Name the blood parasite species.
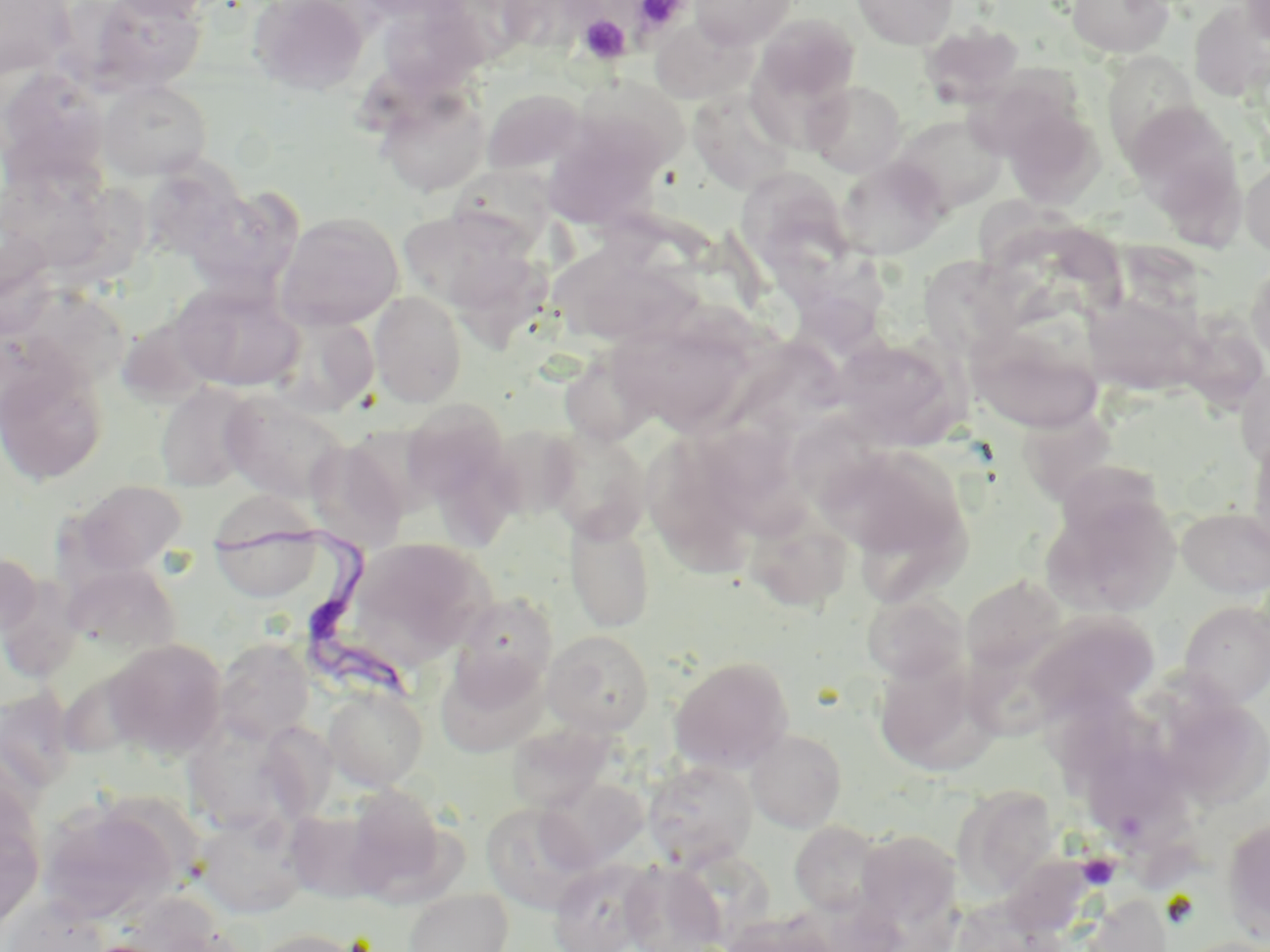

Trypanosoma brucei.

Approximate bounding boxes as named x1/y1/x2/y2 corners in pixels. Uninfected red blood cell locations: (x1=83, y1=0, x2=207, y2=92), (x1=103, y1=0, x2=221, y2=20), (x1=248, y1=0, x2=371, y2=96), (x1=689, y1=0, x2=798, y2=49), (x1=852, y1=0, x2=957, y2=50), (x1=1066, y1=0, x2=1174, y2=58), (x1=1238, y1=0, x2=1270, y2=50), (x1=0, y1=1, x2=75, y2=80), (x1=1189, y1=1, x2=1270, y2=101), (x1=375, y1=3, x2=488, y2=96), (x1=753, y1=13, x2=861, y2=110), (x1=651, y1=20, x2=757, y2=106), (x1=920, y1=23, x2=1024, y2=108), (x1=1101, y1=54, x2=1202, y2=161), (x1=0, y1=67, x2=110, y2=186), (x1=570, y1=75, x2=690, y2=178), (x1=98, y1=80, x2=213, y2=181), (x1=805, y1=80, x2=907, y2=178), (x1=374, y1=85, x2=490, y2=197), (x1=482, y1=88, x2=586, y2=176), (x1=687, y1=88, x2=798, y2=195), (x1=1124, y1=102, x2=1242, y2=212), (x1=1003, y1=105, x2=1105, y2=209), (x1=891, y1=113, x2=1008, y2=215), (x1=541, y1=115, x2=669, y2=229), (x1=835, y1=157, x2=948, y2=261), (x1=1240, y1=158, x2=1270, y2=257), (x1=0, y1=160, x2=118, y2=275), (x1=141, y1=162, x2=247, y2=262), (x1=446, y1=164, x2=559, y2=255), (x1=738, y1=172, x2=856, y2=284), (x1=184, y1=187, x2=301, y2=296), (x1=275, y1=211, x2=404, y2=330), (x1=400, y1=213, x2=547, y2=307), (x1=549, y1=256, x2=699, y2=350), (x1=1246, y1=257, x2=1270, y2=367), (x1=921, y1=262, x2=1057, y2=367), (x1=0, y1=279, x2=143, y2=395), (x1=170, y1=280, x2=304, y2=393), (x1=368, y1=290, x2=468, y2=408), (x1=1085, y1=293, x2=1204, y2=396), (x1=270, y1=311, x2=380, y2=417), (x1=1174, y1=312, x2=1270, y2=412), (x1=974, y1=333, x2=1105, y2=433), (x1=603, y1=336, x2=752, y2=427), (x1=833, y1=336, x2=962, y2=448), (x1=0, y1=359, x2=108, y2=486), (x1=1235, y1=367, x2=1270, y2=472), (x1=154, y1=382, x2=259, y2=492), (x1=219, y1=391, x2=351, y2=504), (x1=399, y1=399, x2=511, y2=512), (x1=1019, y1=416, x2=1131, y2=502), (x1=484, y1=425, x2=582, y2=521), (x1=539, y1=426, x2=653, y2=541), (x1=1247, y1=430, x2=1270, y2=559), (x1=305, y1=439, x2=408, y2=552), (x1=649, y1=441, x2=753, y2=585), (x1=818, y1=443, x2=970, y2=570), (x1=1056, y1=464, x2=1174, y2=551), (x1=67, y1=480, x2=189, y2=578), (x1=1093, y1=493, x2=1186, y2=611), (x1=743, y1=506, x2=855, y2=613), (x1=1177, y1=507, x2=1270, y2=598), (x1=565, y1=514, x2=657, y2=633), (x1=210, y1=517, x2=326, y2=603), (x1=347, y1=537, x2=491, y2=662), (x1=0, y1=553, x2=42, y2=640), (x1=65, y1=563, x2=180, y2=657), (x1=962, y1=575, x2=1068, y2=674), (x1=452, y1=593, x2=558, y2=699), (x1=862, y1=593, x2=967, y2=683), (x1=1180, y1=601, x2=1270, y2=706), (x1=1026, y1=612, x2=1162, y2=722), (x1=543, y1=630, x2=654, y2=735), (x1=214, y1=637, x2=314, y2=743), (x1=105, y1=638, x2=227, y2=759), (x1=873, y1=654, x2=992, y2=775), (x1=670, y1=655, x2=794, y2=772), (x1=441, y1=662, x2=552, y2=759), (x1=0, y1=686, x2=78, y2=795), (x1=322, y1=686, x2=428, y2=790), (x1=1045, y1=691, x2=1171, y2=786), (x1=183, y1=718, x2=305, y2=835), (x1=257, y1=720, x2=338, y2=824), (x1=508, y1=724, x2=613, y2=812), (x1=745, y1=728, x2=847, y2=833), (x1=1084, y1=743, x2=1191, y2=837), (x1=643, y1=759, x2=757, y2=869), (x1=537, y1=777, x2=648, y2=873), (x1=951, y1=784, x2=1060, y2=900), (x1=338, y1=786, x2=453, y2=902), (x1=0, y1=792, x2=45, y2=934), (x1=37, y1=798, x2=182, y2=925), (x1=482, y1=801, x2=594, y2=914), (x1=284, y1=808, x2=388, y2=904), (x1=194, y1=809, x2=310, y2=919), (x1=1222, y1=816, x2=1270, y2=941), (x1=789, y1=821, x2=887, y2=916), (x1=856, y1=829, x2=961, y2=929), (x1=548, y1=858, x2=659, y2=952), (x1=619, y1=860, x2=727, y2=952), (x1=404, y1=888, x2=513, y2=952), (x1=2, y1=896, x2=109, y2=952), (x1=721, y1=914, x2=838, y2=952), (x1=248, y1=928, x2=369, y2=952). Platelet locations: (x1=631, y1=1, x2=690, y2=37), (x1=578, y1=14, x2=632, y2=64), (x1=1077, y1=853, x2=1119, y2=890). Trypanosoma brucei locations: (x1=212, y1=525, x2=418, y2=709). Captured at 1000x magnification. Single field of view. Thin blood film. Optical microscopy. Image is 1270×952 pixels. May-Grünwald-Giemsa stain.